Describe the morphology of the red blood cells.
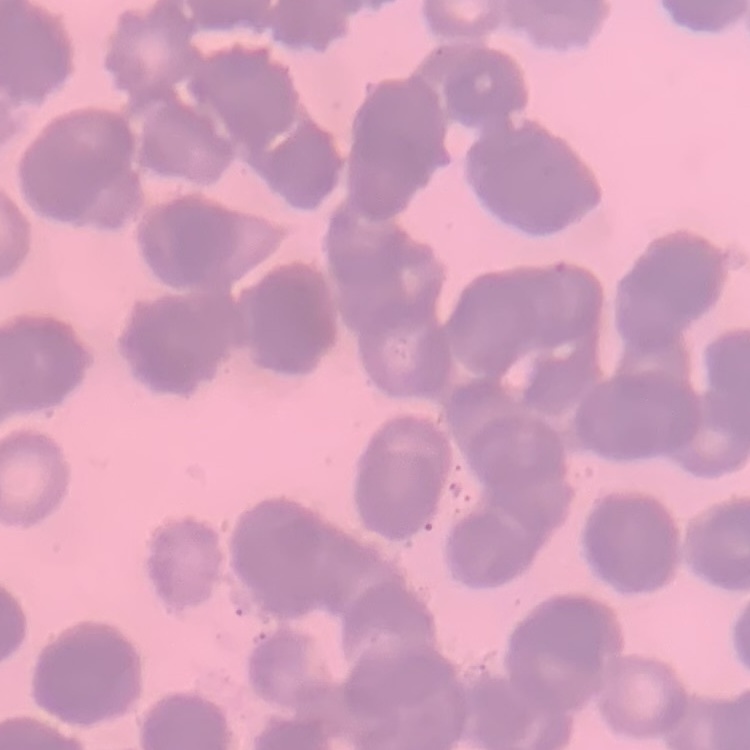

Rouleaux formation.

Summary:
  - Preparation: thin blood film
  - Image type: square crop of a larger photomicrograph
  - Stain: Field's or Giemsa